Give the extent of all Plasmodium falciparum-infected red blood cells.
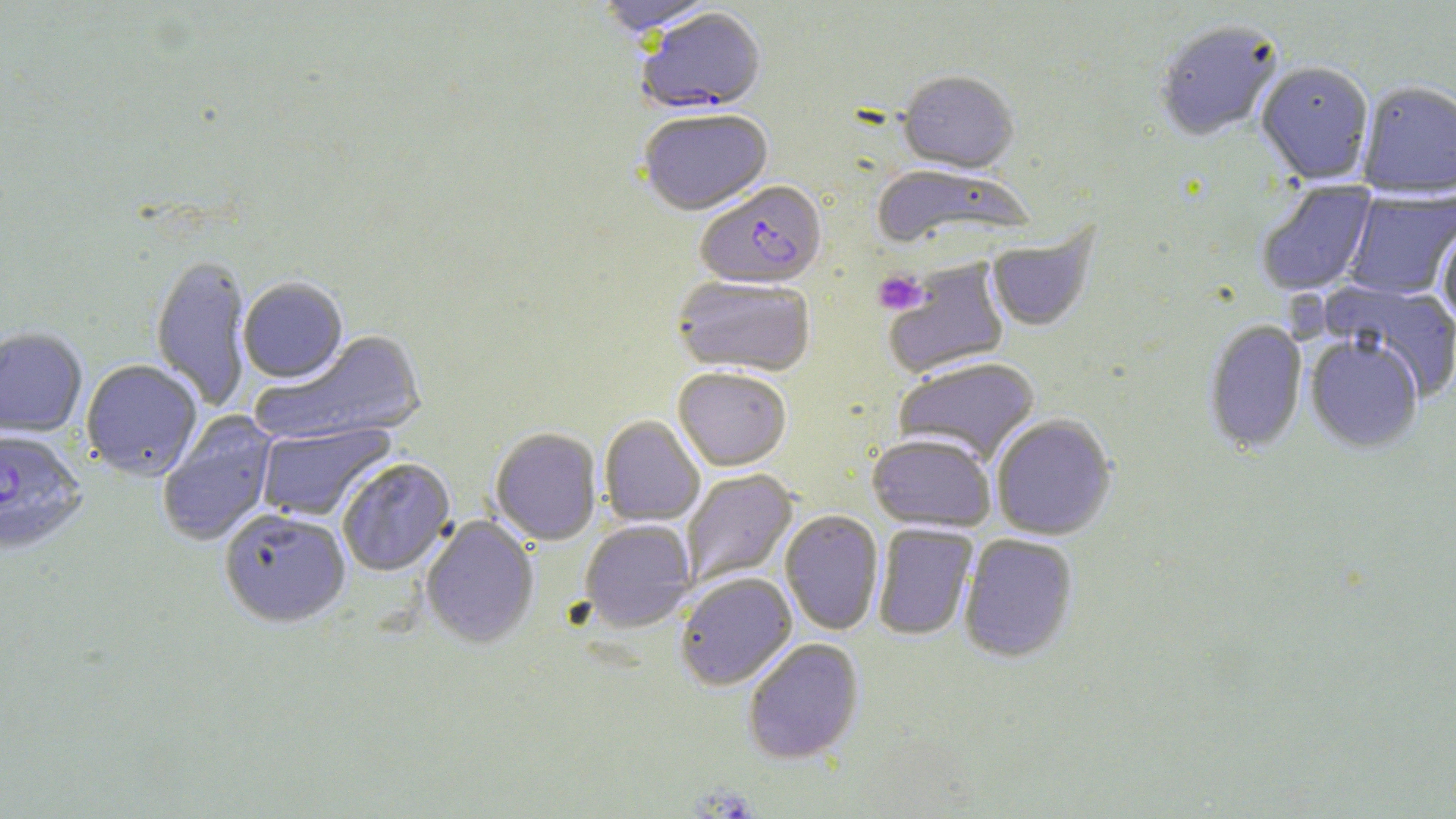

Approximate bounding boxes as [x1, y1, x2, y2] in pixels.
Plasmodium falciparum-infected red blood cells: [637, 9, 766, 116], [696, 183, 827, 291], [0, 430, 87, 555].

slide-level diagnosis = Plasmodium falciparum
uninfected red blood cell locations = approximate bounding boxes as [x1, y1, x2, y2] in pixels: [594, 0, 719, 38], [1153, 21, 1285, 143], [1255, 63, 1374, 185], [897, 72, 1019, 176], [1356, 83, 1456, 199], [638, 110, 774, 217], [870, 166, 1034, 248], [1255, 180, 1378, 297], [1343, 189, 1456, 301], [1437, 221, 1456, 325], [986, 225, 1099, 333], [150, 255, 251, 413], [883, 259, 1010, 378], [672, 276, 815, 376], [238, 278, 348, 384], [1321, 280, 1456, 402], [1203, 320, 1308, 455], [0, 328, 88, 437], [251, 330, 428, 448], [1305, 335, 1423, 454], [893, 357, 1041, 465], [80, 360, 203, 480], [673, 367, 792, 471], [157, 411, 279, 547], [991, 414, 1116, 540], [599, 415, 705, 526], [255, 421, 395, 522], [490, 428, 602, 546], [867, 433, 996, 532], [337, 458, 455, 577], [682, 469, 798, 586], [218, 508, 351, 629], [780, 510, 884, 636], [421, 515, 539, 649], [579, 520, 696, 632], [873, 523, 978, 640], [959, 534, 1078, 663], [675, 572, 796, 690], [743, 638, 864, 764]
preparation = thin blood film
field of view = one of a larger specimen
magnification = 1000x
platelet locations = approximate bounding boxes as [x1, y1, x2, y2] in pixels: [874, 269, 928, 315]
modality = optical microscopy
image size = 1456×819 pixels
stain = May-Grünwald-Giemsa